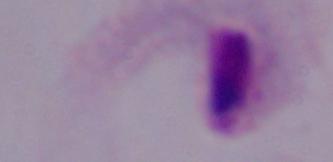

Summary:
  - Identification: trichomonad
  - Magnification: 1000x
  - Modality: photomicrograph